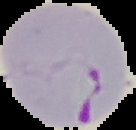 Segmented cell region on a black background. Result: malaria parasites detected. Image is 136×130 pixels. From a thin blood film.